Describe the morphology of the erythrocytes.
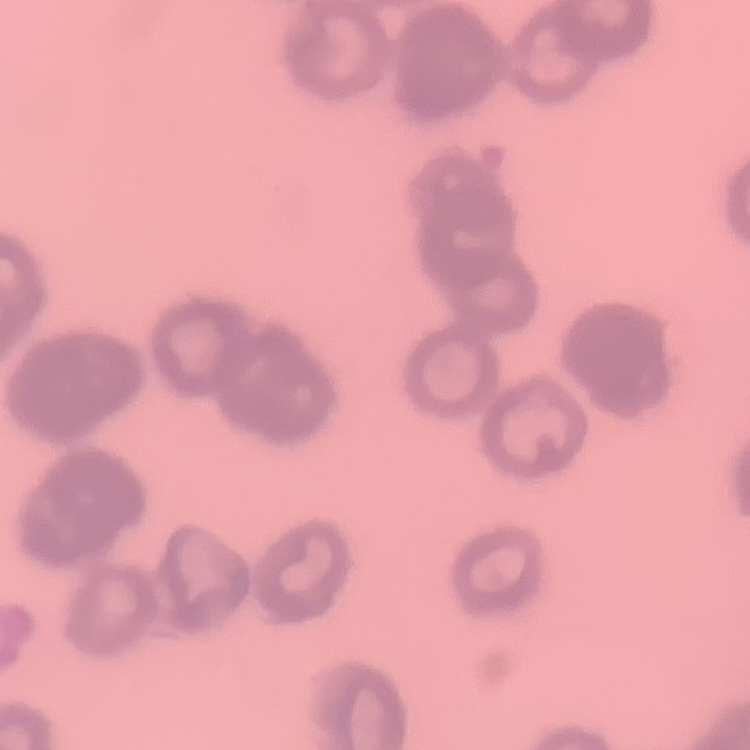

They show rouleaux formation.

preparation: thin peripheral smear
image_type: square crop of a larger photomicrograph
stain: Field's or Giemsa